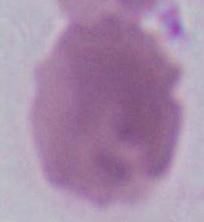

identification = erythrocyte
magnification = 1000x
modality = micrograph